Evaluate for malaria.
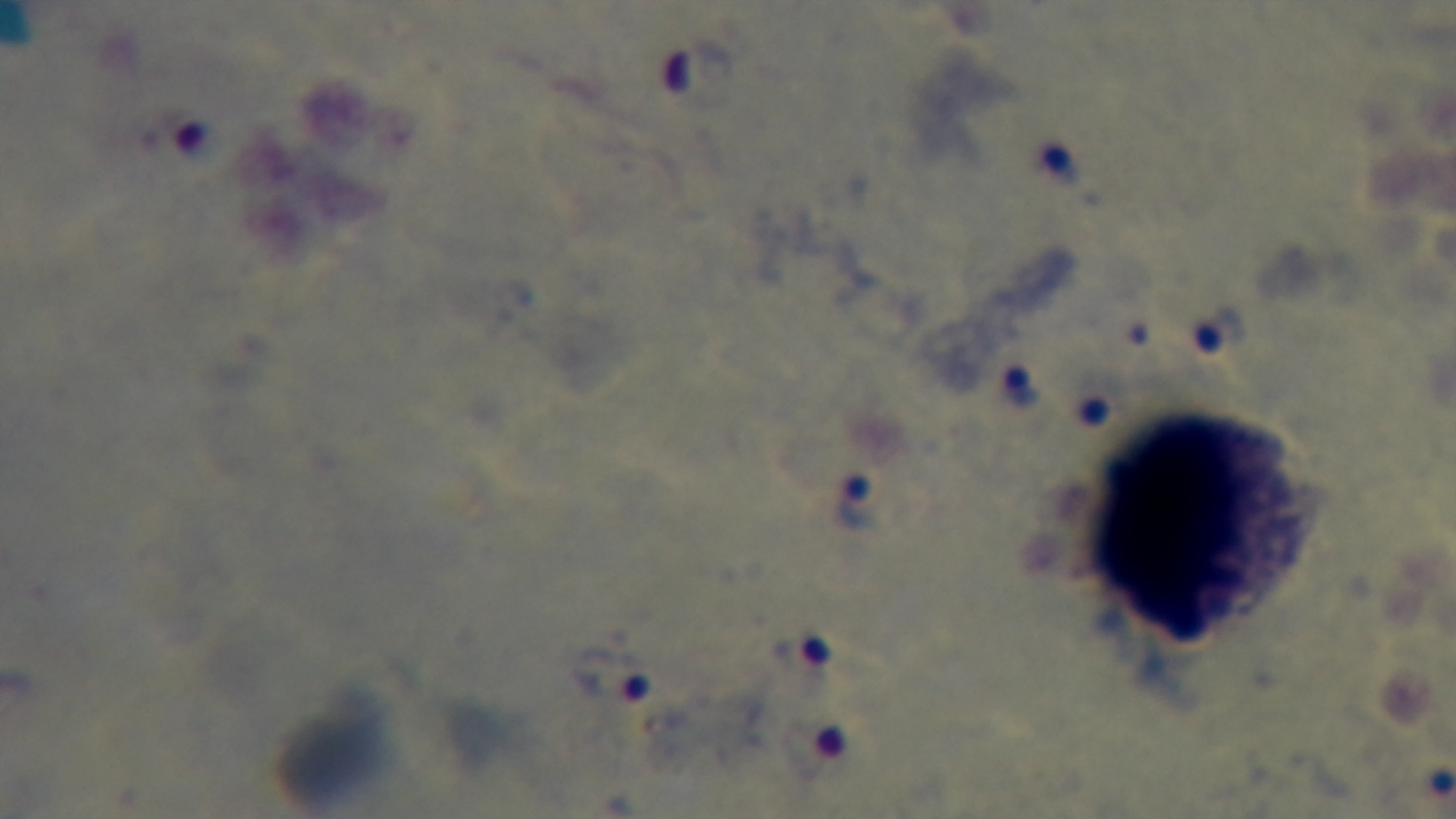
Positive.

Summary:
  - Preparation: thick smear
  - Objective: 100x oil immersion
  - Capture: mounted 4K digital camera
  - Stain: Giemsa
  - Field of view: single
  - Modality: light microscopy